Assess the morphology of the red blood cells.
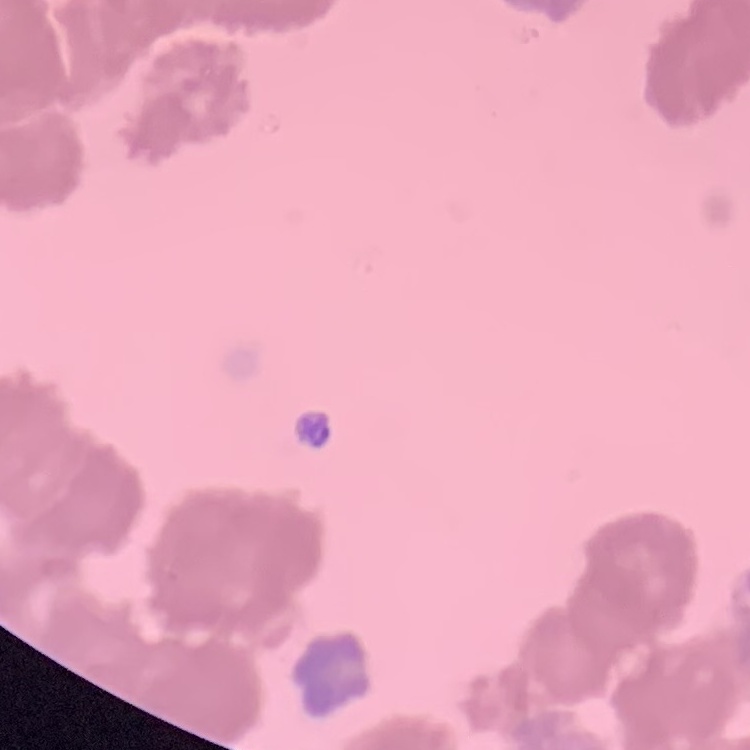
Rouleaux formation.

Field's or Giemsa stain. Thin blood smear. One tile cut from a larger photomicrograph.